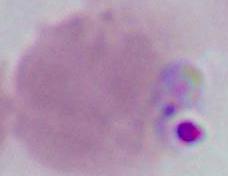

A red blood cell is seen. Photomicrograph. Captured at 1000x magnification.